Locate and identify every blood parasite.
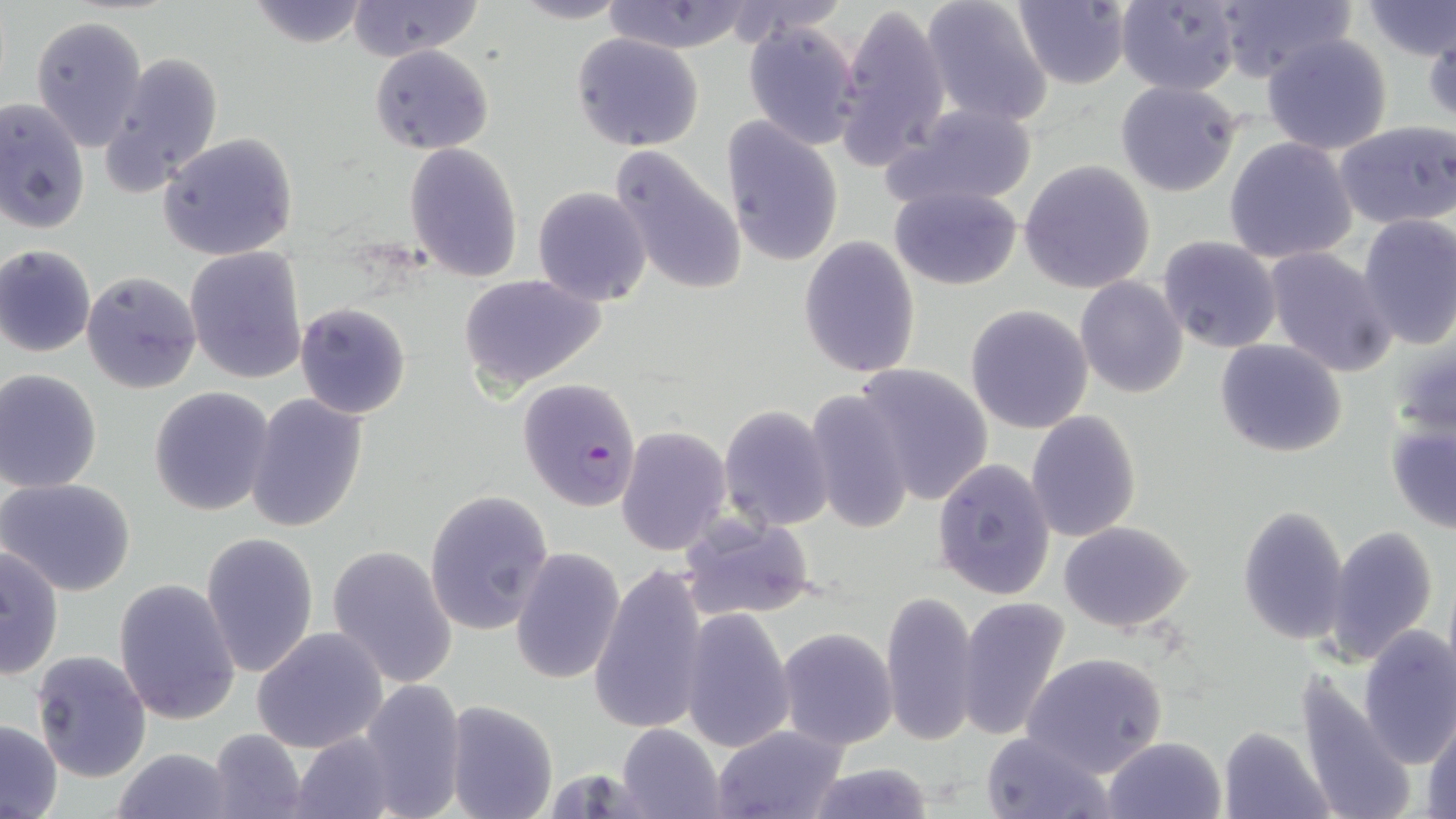
Approximate bounding boxes as named x1/y1/x2/y2 corners in pixels.
Plasmodium falciparum-infected red blood cells: (x1=517, y1=377, x2=644, y2=513).
No Plasmodium ovale, Plasmodium malariae, Plasmodium vivax, Babesia divergens, or Trypanosoma brucei observed.

Summary:
  - Uninfected red blood cell locations: (x1=244, y1=0, x2=372, y2=48), (x1=346, y1=0, x2=481, y2=60), (x1=921, y1=0, x2=1053, y2=127), (x1=1114, y1=0, x2=1244, y2=95), (x1=1356, y1=0, x2=1456, y2=62), (x1=510, y1=1, x2=631, y2=24), (x1=602, y1=1, x2=757, y2=52), (x1=1011, y1=1, x2=1131, y2=88), (x1=1214, y1=1, x2=1351, y2=84), (x1=835, y1=2, x2=952, y2=166), (x1=32, y1=15, x2=147, y2=150), (x1=740, y1=19, x2=861, y2=150), (x1=1424, y1=22, x2=1456, y2=129), (x1=572, y1=32, x2=705, y2=152), (x1=1261, y1=32, x2=1394, y2=155), (x1=369, y1=45, x2=493, y2=155), (x1=101, y1=51, x2=224, y2=196), (x1=1115, y1=80, x2=1243, y2=198), (x1=0, y1=99, x2=90, y2=234), (x1=887, y1=102, x2=1039, y2=210), (x1=722, y1=117, x2=844, y2=269), (x1=1334, y1=121, x2=1456, y2=229), (x1=158, y1=132, x2=299, y2=262), (x1=1224, y1=137, x2=1357, y2=265), (x1=403, y1=143, x2=523, y2=283), (x1=609, y1=144, x2=746, y2=299), (x1=1019, y1=159, x2=1155, y2=295), (x1=532, y1=185, x2=652, y2=304), (x1=888, y1=185, x2=1023, y2=290), (x1=1355, y1=214, x2=1456, y2=349), (x1=1157, y1=235, x2=1285, y2=354), (x1=799, y1=236, x2=921, y2=379), (x1=0, y1=245, x2=97, y2=357), (x1=185, y1=246, x2=309, y2=385), (x1=1263, y1=247, x2=1397, y2=377), (x1=81, y1=270, x2=202, y2=395), (x1=459, y1=273, x2=607, y2=391), (x1=1075, y1=277, x2=1189, y2=399), (x1=294, y1=302, x2=410, y2=419), (x1=965, y1=304, x2=1095, y2=433), (x1=1214, y1=338, x2=1348, y2=458), (x1=853, y1=363, x2=995, y2=506), (x1=0, y1=369, x2=104, y2=493), (x1=148, y1=388, x2=274, y2=516), (x1=803, y1=393, x2=916, y2=532), (x1=246, y1=394, x2=369, y2=533), (x1=718, y1=404, x2=835, y2=532), (x1=1026, y1=410, x2=1142, y2=543), (x1=1384, y1=416, x2=1454, y2=534), (x1=617, y1=425, x2=731, y2=556), (x1=931, y1=458, x2=1056, y2=599), (x1=1, y1=478, x2=136, y2=596), (x1=424, y1=489, x2=554, y2=636), (x1=1236, y1=505, x2=1350, y2=646), (x1=679, y1=515, x2=816, y2=622), (x1=1058, y1=520, x2=1194, y2=635), (x1=1323, y1=525, x2=1441, y2=663), (x1=201, y1=531, x2=319, y2=680), (x1=1, y1=544, x2=67, y2=682), (x1=326, y1=545, x2=458, y2=689), (x1=512, y1=547, x2=625, y2=687), (x1=588, y1=562, x2=710, y2=735), (x1=113, y1=579, x2=241, y2=724), (x1=880, y1=591, x2=979, y2=748), (x1=955, y1=597, x2=1071, y2=742), (x1=679, y1=608, x2=795, y2=752), (x1=1356, y1=625, x2=1456, y2=769), (x1=777, y1=626, x2=899, y2=750), (x1=253, y1=627, x2=388, y2=753), (x1=32, y1=651, x2=152, y2=783), (x1=1023, y1=651, x2=1170, y2=776), (x1=1293, y1=670, x2=1417, y2=819), (x1=357, y1=680, x2=467, y2=818), (x1=443, y1=700, x2=558, y2=819), (x1=1423, y1=713, x2=1456, y2=818), (x1=0, y1=719, x2=63, y2=818), (x1=615, y1=724, x2=725, y2=818), (x1=711, y1=726, x2=848, y2=819), (x1=1218, y1=726, x2=1333, y2=818), (x1=204, y1=728, x2=307, y2=816), (x1=980, y1=731, x2=1112, y2=819), (x1=290, y1=732, x2=401, y2=818), (x1=1102, y1=736, x2=1228, y2=819), (x1=111, y1=746, x2=238, y2=818), (x1=800, y1=764, x2=937, y2=819)
  - Slide-level diagnosis: Plasmodium falciparum
  - Stain: May-Grünwald-Giemsa
  - Field of view: single
  - Image size: 1456×819 pixels
  - Magnification: 1000x
  - Preparation: thin blood film
  - Modality: optical microscopy